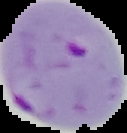
preparation = thin blood film
image size = 127×133 pixels
image type = segmented cell region on a black background
result = malaria parasites identified